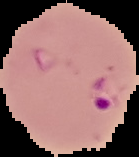

Summary:
  - Malaria status: parasitized
  - Image type: segmented cell region on a black background
  - Image size: 139×157 pixels
  - Preparation: thin blood film